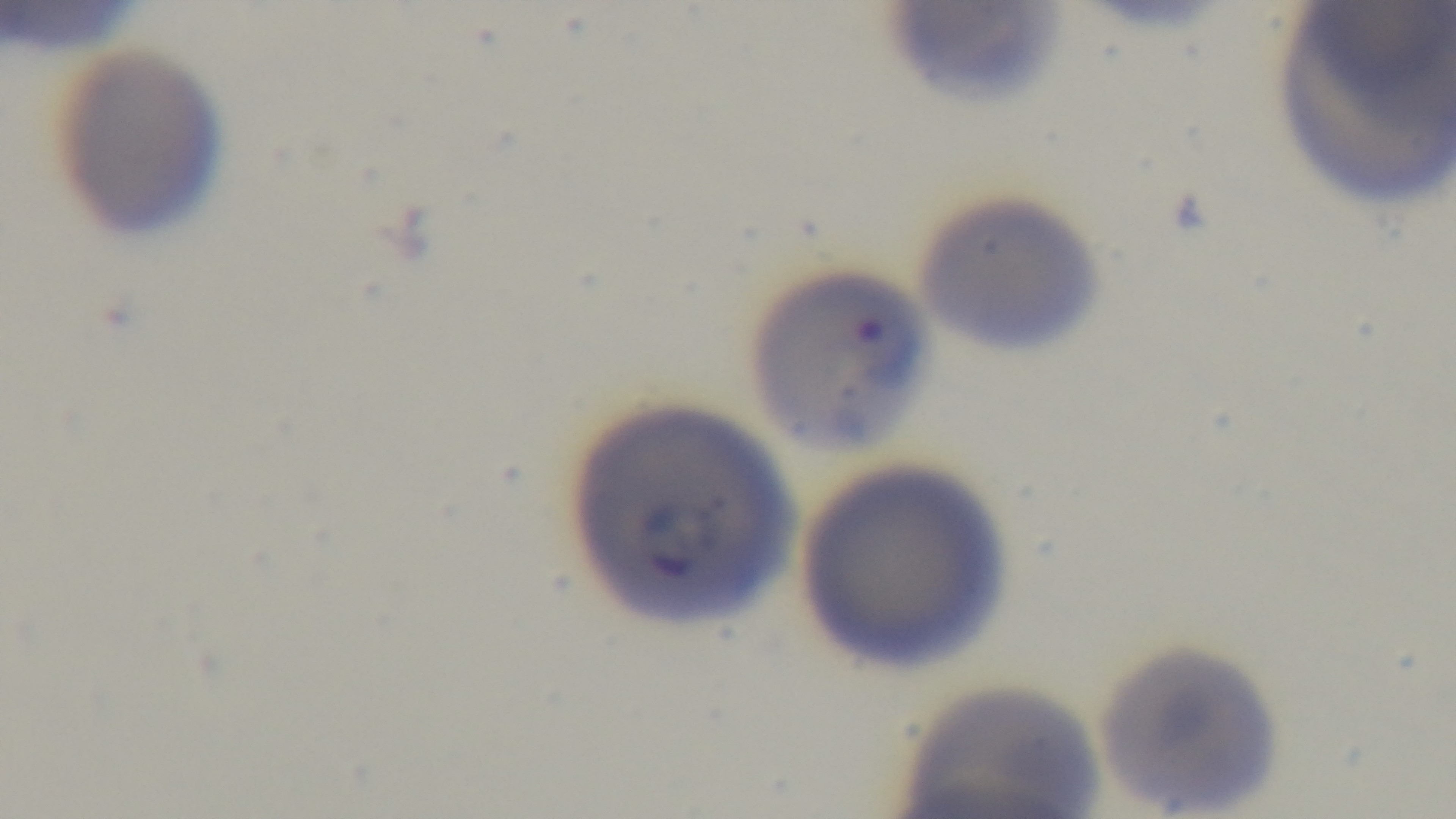
Summary:
  - Preparation: thin smear
  - Modality: light microscopy
  - Objective: 100x oil immersion
  - Malaria status: positive
  - Field of view: one from the slide
  - Capture: mounted 4K digital camera
  - Stain: Giemsa